Name the blood parasite species.
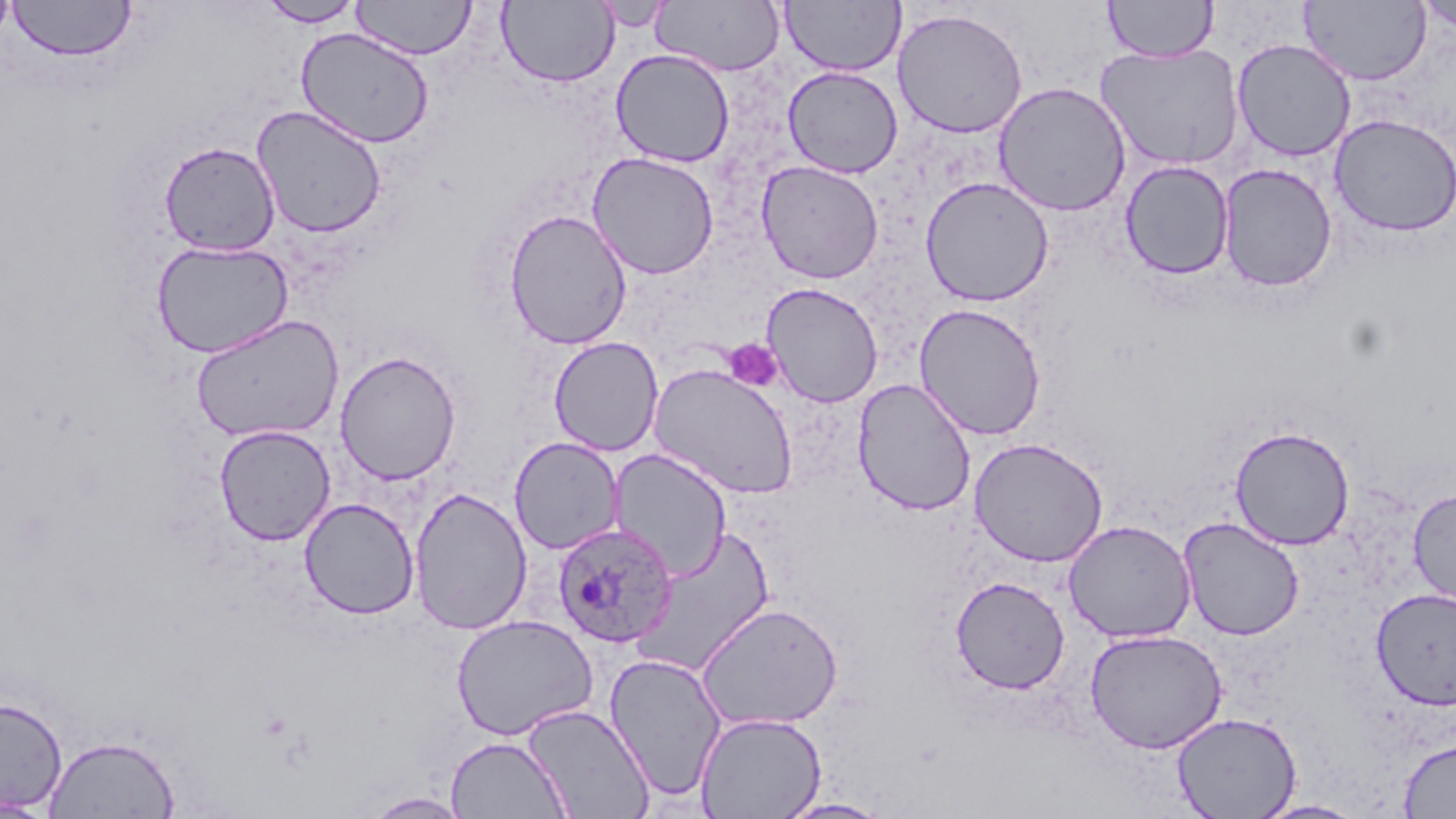

Plasmodium ovale.

Approximate bounding boxes as (x1,y1)-(x2,y2) corner pairs in pixels. Uninfected red blood cell locations: (0,0)-(16,51), (257,0)-(365,27), (352,0)-(477,60), (652,0)-(785,76), (780,0)-(905,77), (1103,0)-(1219,62), (1299,0)-(1432,86), (1415,0)-(1456,37), (7,1)-(137,62), (497,1)-(620,88), (593,3)-(675,32), (892,8)-(1028,139), (295,27)-(434,147), (1231,38)-(1357,162), (1097,43)-(1244,171), (610,49)-(735,168), (782,66)-(903,178), (993,81)-(1131,217), (250,105)-(388,239), (1329,113)-(1456,238), (159,141)-(281,256), (586,151)-(720,280), (756,160)-(884,284), (1120,160)-(1235,281), (1218,163)-(1338,292), (920,176)-(1055,307), (503,209)-(633,350), (151,239)-(294,359), (760,282)-(884,408), (913,303)-(1047,440), (190,314)-(344,444), (548,336)-(663,457), (334,350)-(462,485), (647,363)-(800,499), (852,377)-(977,516), (213,425)-(336,545), (1229,425)-(1355,550), (509,436)-(625,555), (969,437)-(1108,567), (608,448)-(732,580), (1407,485)-(1456,610), (408,487)-(533,635), (299,497)-(420,619), (1177,517)-(1305,641), (1062,519)-(1197,643), (636,525)-(777,675), (950,576)-(1070,694), (1370,588)-(1456,709), (696,602)-(844,731), (451,614)-(598,740), (1085,628)-(1228,753), (605,652)-(727,801), (0,697)-(68,812), (522,702)-(655,819), (694,711)-(827,819), (1171,711)-(1302,819), (43,734)-(181,818), (445,735)-(571,818), (1398,738)-(1456,817), (363,792)-(472,818), (0,796)-(52,817), (775,798)-(893,818), (1252,799)-(1369,819). Plasmodium ovale-infected red blood cell locations: (551,522)-(679,647). Platelet locations: (722,338)-(783,392). Image is 1456×819 pixels. Single field of view. Thin blood smear. May-Grünwald-Giemsa stain. Light microscopy. 1000x magnification.